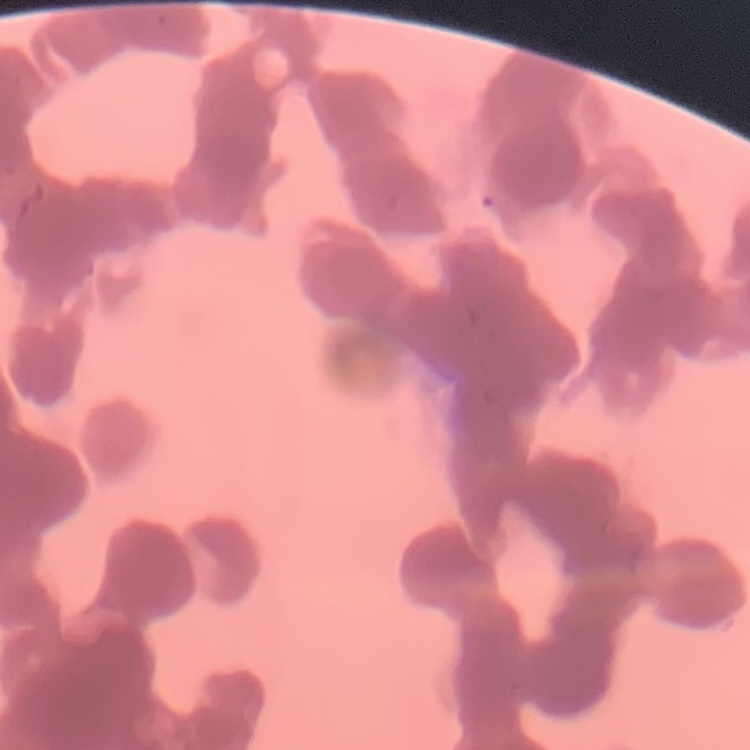

Summary:
  - Erythrocyte morphology: rouleaux formation
  - Preparation: thin blood film
  - Stain: Field's or Giemsa
  - Image type: one tile cut from a larger photomicrograph